Describe the morphology of the erythrocytes.
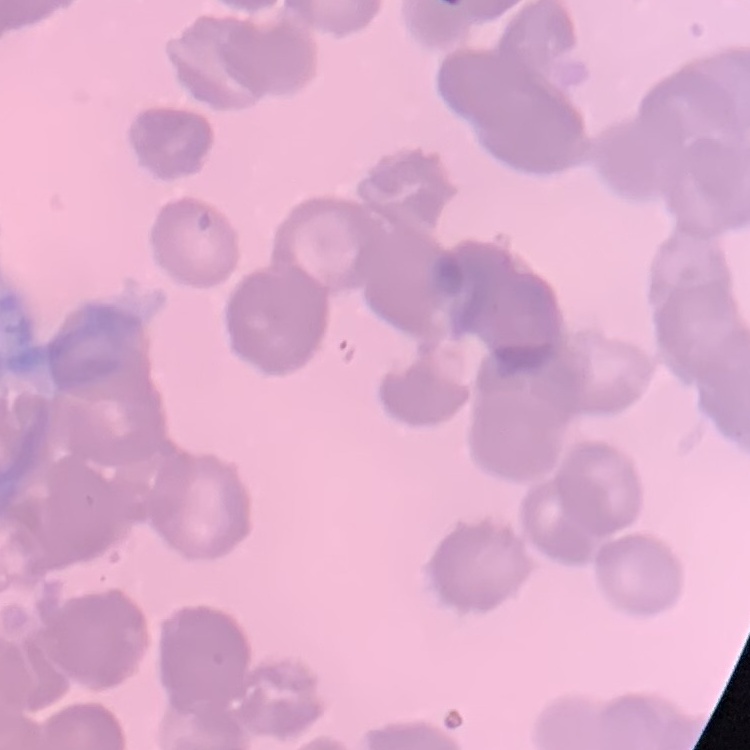
They show rouleaux formation.

One tile cut from a larger photomicrograph. Field's or Giemsa stain. Thin blood smear.